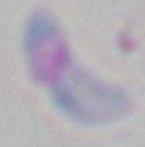
identification: Toxoplasma gondii
magnification: 1000x
modality: photomicrograph